Assess for parasitized red blood cells.
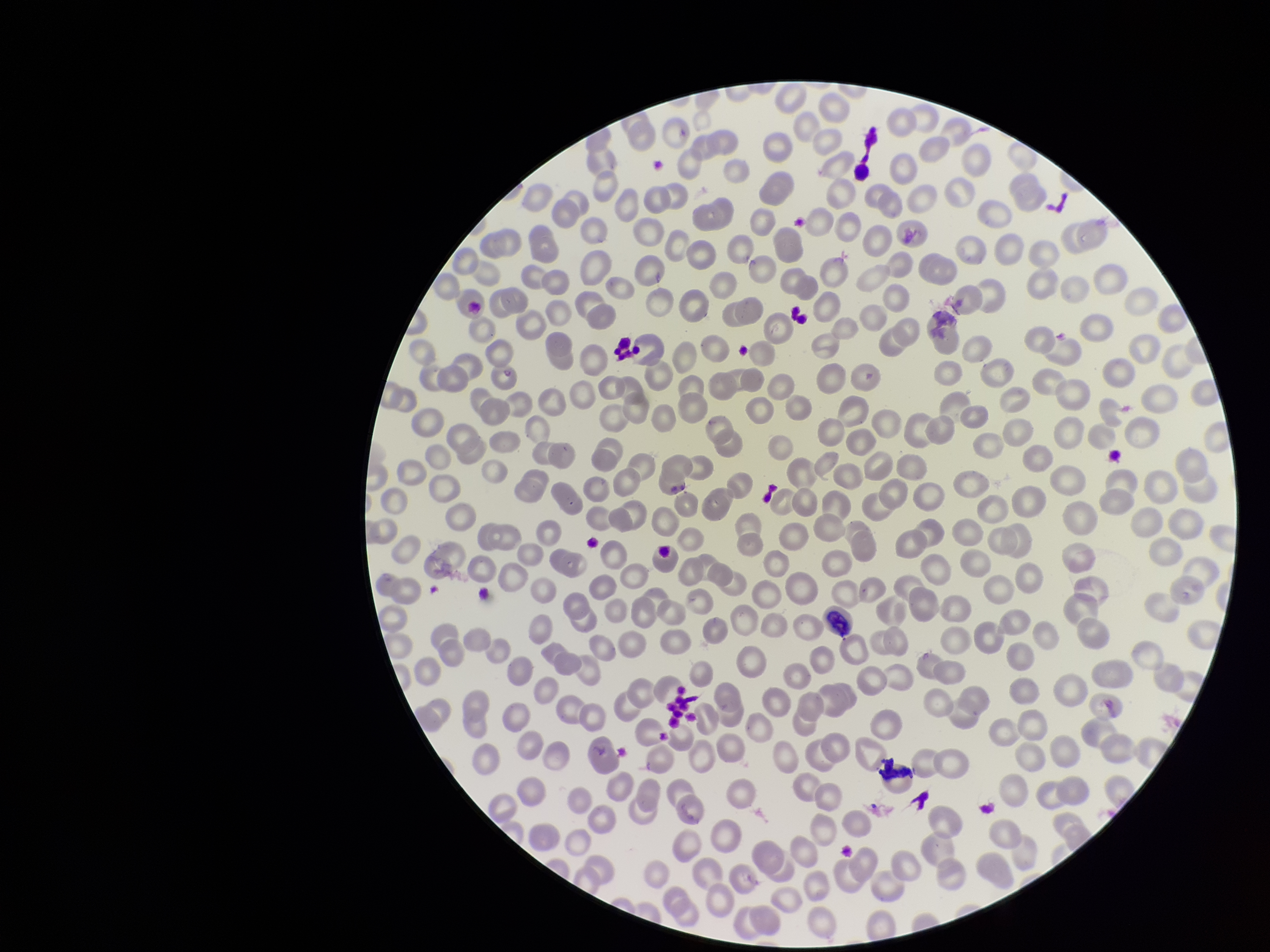

None detected.

Patient malaria status: negative. Stained with Giemsa. Parasitized red blood cell count: 0. Photographed through the microscope eyepiece with a smartphone camera. Preparation: thin smear. Image is 1270×952 pixels. Red blood cell count: 268. One field from this slide.